Point out malaria parasites and leukocytes.
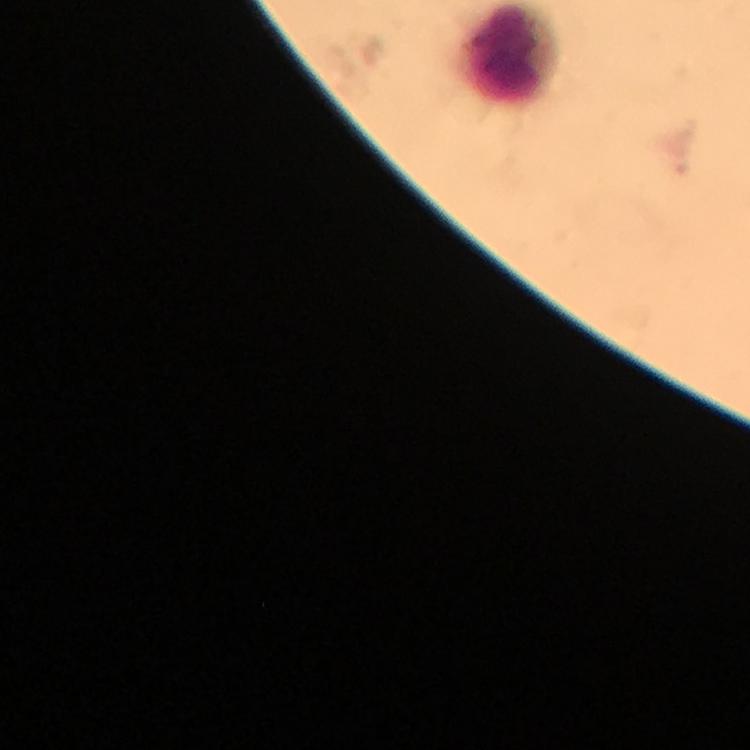
No malaria parasites detected.
Approximate centers as (x, y) in pixels.
Leukocytes: (510, 55).

magnification = 100x
preparation = thick blood film
stain = Giemsa
cropped from = one field of view
immersion oil = used
capture = smartphone camera through the microscope
image size = 750×750 pixels
context = from a malaria diagnostic workup